Locate every malaria parasite.
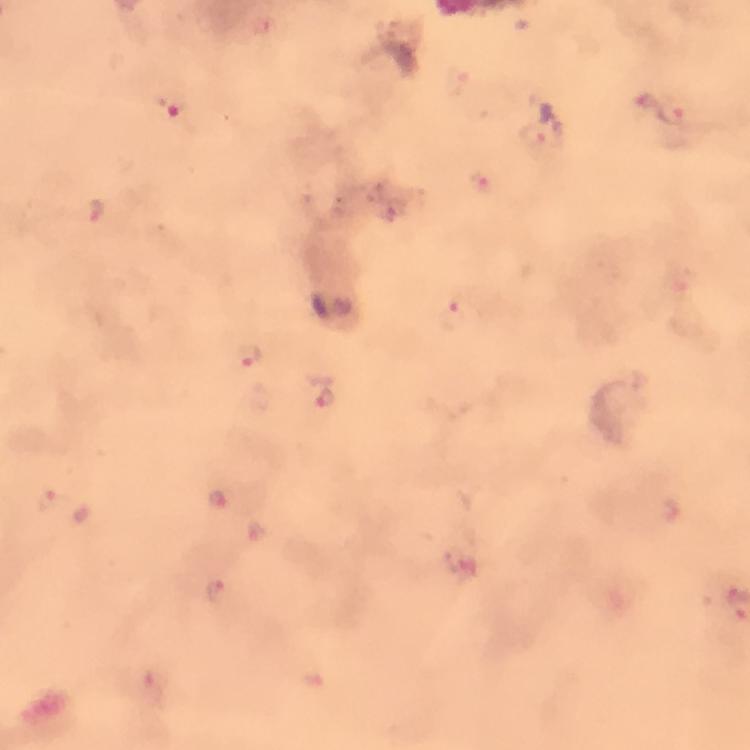

Approximate centers as [x, y] in pixels.
Malaria parasites: [458, 82], [175, 104], [675, 114], [544, 136], [482, 185], [97, 215], [459, 314], [250, 357], [324, 397], [52, 500], [217, 501], [256, 532], [464, 560], [216, 593], [153, 689].

stain: Giemsa
magnification: 100x
cropped_from: a single field of view
capture: smartphone photograph through a microscope
immersion_oil: applied
image_size: 750×750 pixels
preparation: thick blood smear
context: from a malaria diagnostic workup